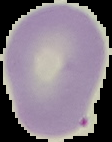
Summary:
  - Preparation: thin blood smear
  - Image type: segmented cell region with the area outside set to black
  - Result: negative for malaria parasites
  - Image size: 112×142 pixels